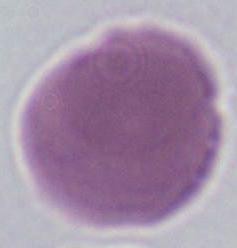
{
  "magnification": "1000x",
  "modality": "micrograph",
  "identification": "red blood cell"
}